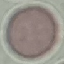
Malaria status: uninfected. Thin blood film. Giemsa stain. Automatically extracted cell patch, resized to 64 × 64 pixels. Photographed with a smartphone camera at the microscope eyepiece.